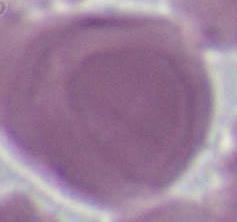

{
  "magnification": "1000x",
  "identification": "red blood cell",
  "modality": "photomicrograph"
}